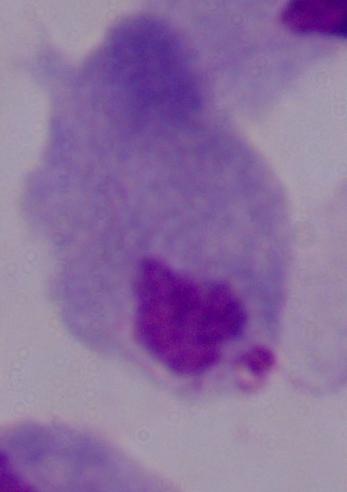

Captured at 1000x magnification. Photomicrograph. A trichomonad is seen.